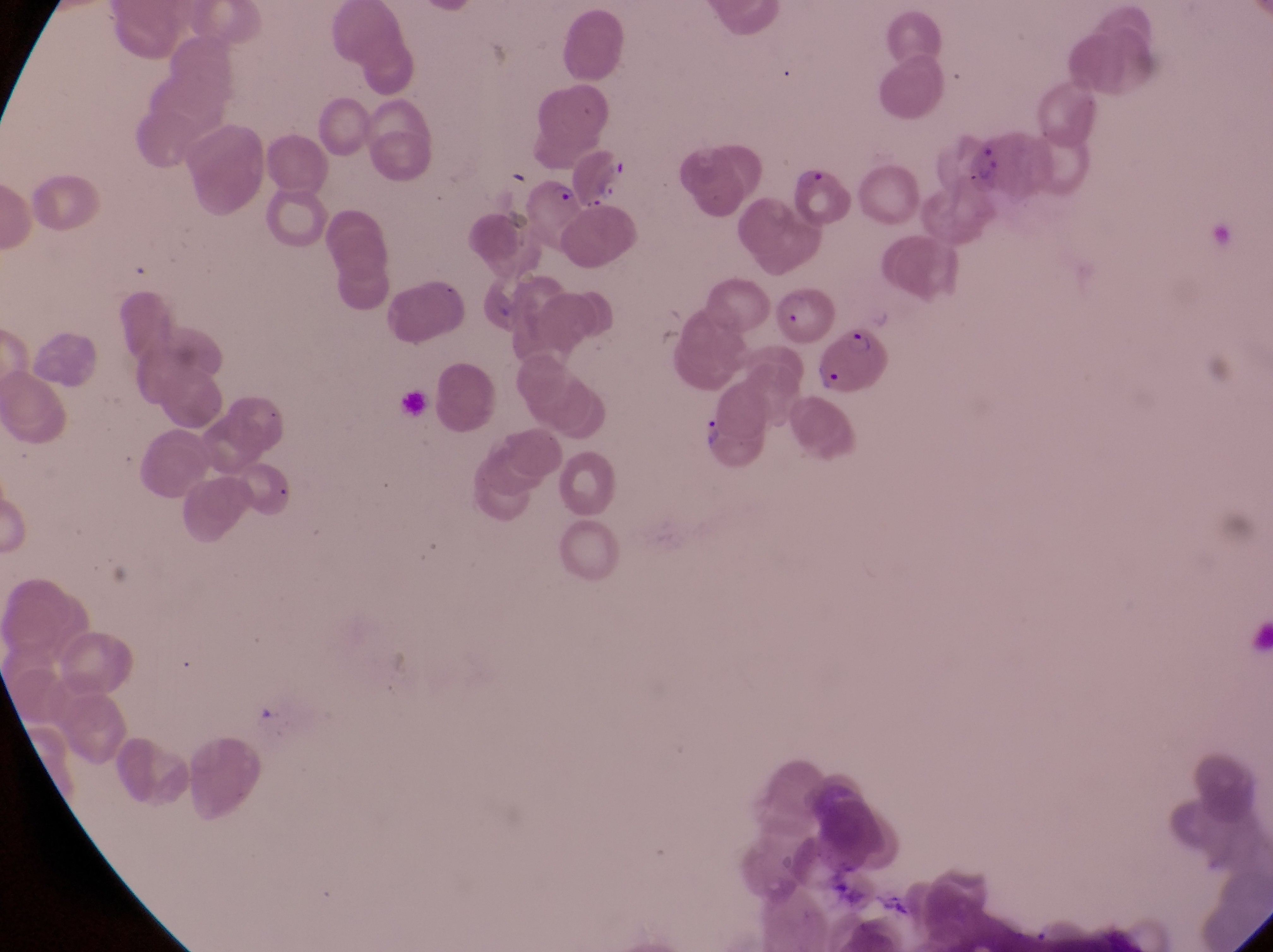
{
  "capture": "smartphone photograph through the eyepiece of an Olympus CX-23 microscope",
  "magnification": "1000x",
  "parasitised_red_blood_cell_locations": "approximate bounding boxes as left top right bottom in pixels: 787 163 857 229; 527 175 582 238; 814 322 897 399",
  "preparation": "thin blood film",
  "trophozoite_locations": "approximate bounding boxes as left top right bottom in pixels: 973 148 1005 183; 597 175 629 207; 704 415 726 454",
  "country": "Uganda",
  "field_of_view": "single",
  "image_size": "1273×952 pixels"
}